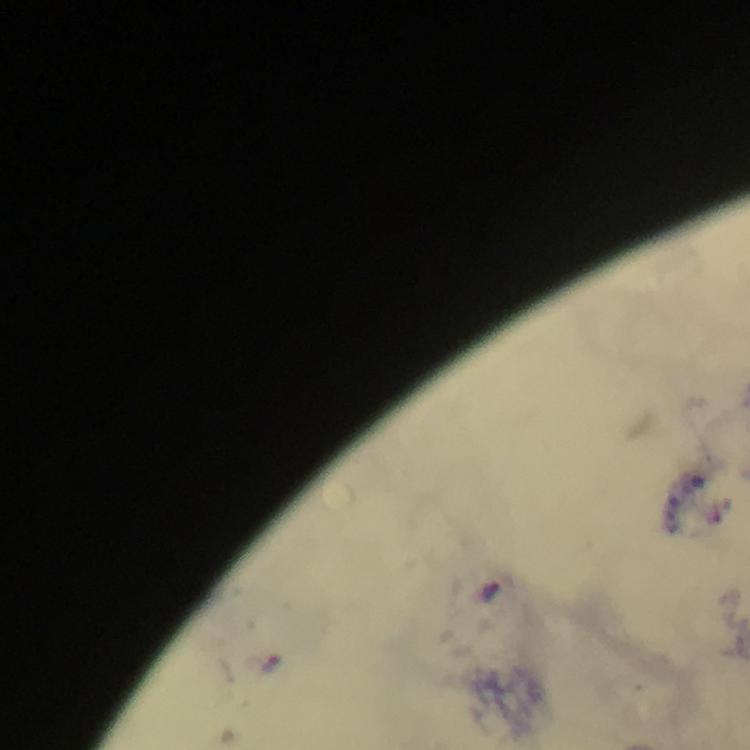
Approximate centers as {x, y} in pixels. Malaria parasite locations: {272, 665}. Photographed through the microscope with a smartphone camera. From a malaria diagnostic workup. A crop from one field of view. At 100x magnification. Thick smear. Immersion oil was used. Giemsa stain. Image is 750×750 pixels.